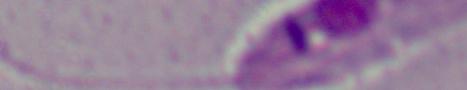

{
  "modality": "micrograph",
  "magnification": "1000x",
  "identification": "Leishmania"
}